Report the malaria status of this cell.
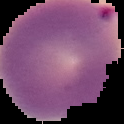

Parasitized.

Summary:
  - Image size: 124×124 pixels
  - Image type: cell region segmented out of the field of view; surrounding area masked to black
  - Preparation: thin blood film